Assess the morphology of the erythrocytes.
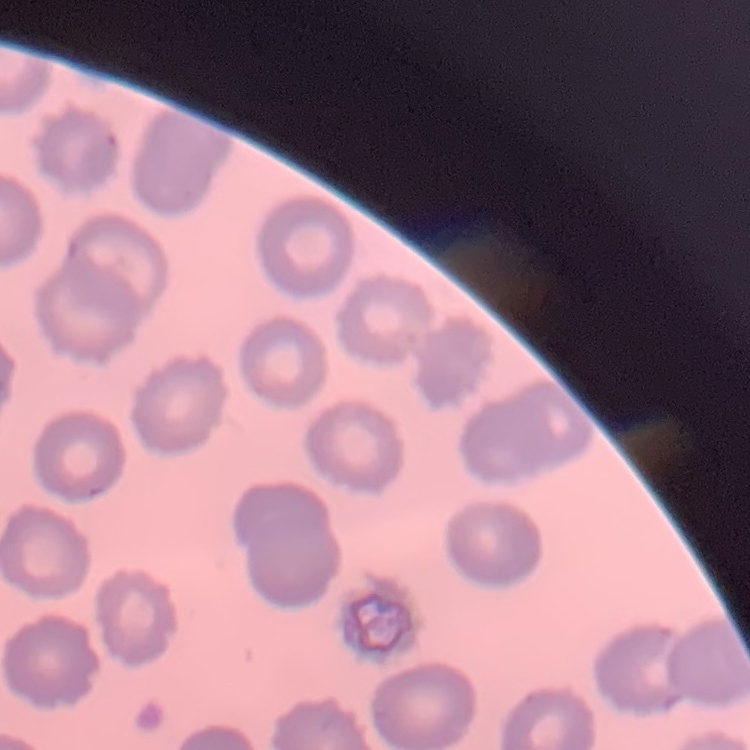

They show no rouleaux formation.

One tile cut from a larger photomicrograph. Stained with either Field's or Giemsa. Thin peripheral smear.